Name the parasite shown.
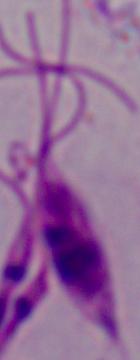

This is Leishmania.

modality = photomicrograph
magnification = 1000x